Locate every malaria parasite.
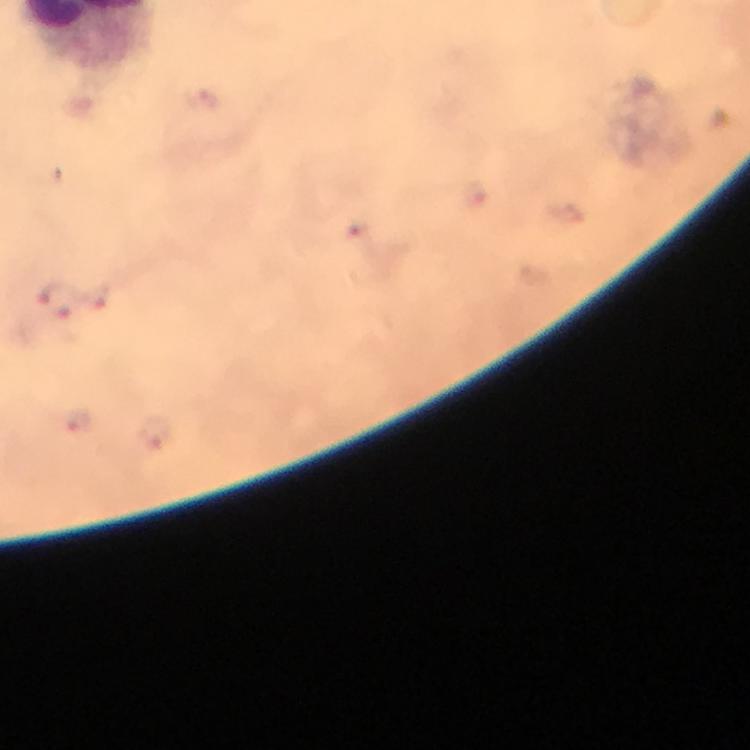

Approximate centers as {x, y} in pixels.
Malaria parasites: {100, 296}, {58, 300}, {78, 419}, {156, 432}.

Image is 750×750 pixels. Smartphone photograph taken through a microscope. At 100x magnification. Thick smear. Immersion oil applied. A crop from one field of view. Giemsa stain. From a malaria diagnostic workup.